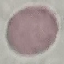
Result: no malaria parasites detected. Acquired by smartphone through the microscope eyepiece. Cell patch, automatically extracted from a larger field of view and resized to 64 × 64 pixels. Giemsa-stained preparation. Thin blood film.